Assess this cell for malaria.
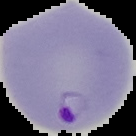
Parasitized.

Summary:
  - Preparation: thin blood smear
  - Image size: 136×136 pixels
  - Image type: cell region segmented out of the field of view; surrounding area masked to black